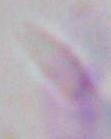
magnification: 1000x
identification: Toxoplasma gondii
modality: photomicrograph